Assess this cell for malaria.
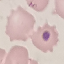
It is uninfected.

image type = cell patch, automatically extracted from a larger field of view and resized to 64 × 64 pixels
capture = smartphone through the microscope eyepiece
stain = Giemsa
preparation = thin blood film